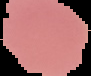

image type = cell region segmented out of the field of view; surrounding area masked to black
preparation = thin blood film
malaria status = uninfected
image size = 91×76 pixels